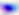
modality = micrograph
magnification = 400x
identification = Toxoplasma gondii